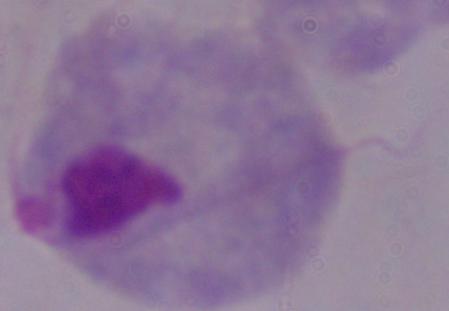

Summary:
  - Identification: trichomonad
  - Modality: photomicrograph
  - Magnification: 1000x